State which cell type is depicted.
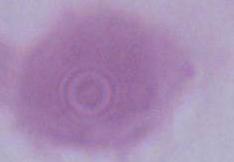

This is an erythrocyte.

1000x magnification. Photomicrograph.